Report the malaria status of this cell.
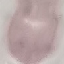
It is uninfected.

Summary:
  - Preparation: thin blood smear
  - Stain: Giemsa
  - Capture: smartphone camera at the microscope eyepiece
  - Image type: automatically extracted cell patch, resized to 64 × 64 pixels